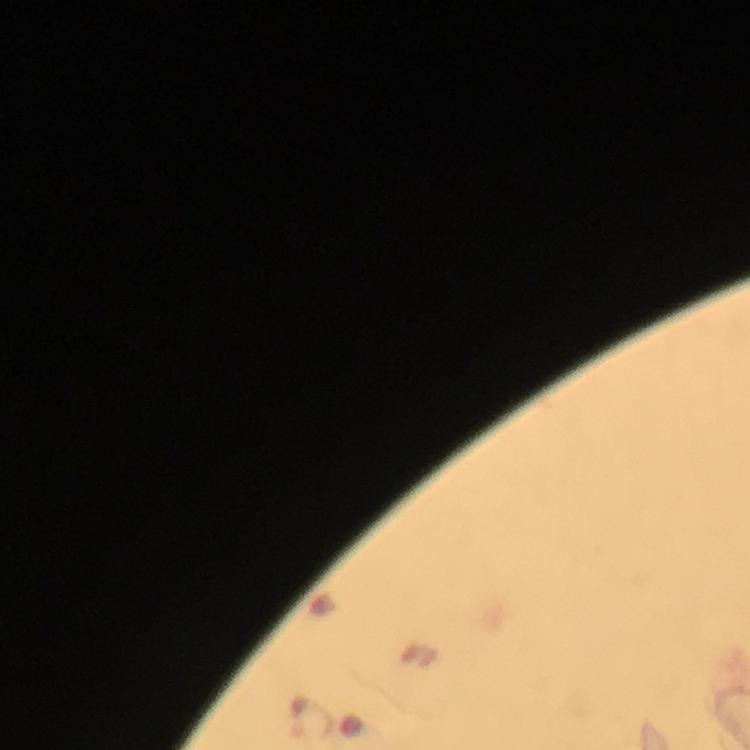
Approximate object centers, in pixels from the top-left corner.
Summary:
  - Malaria parasite locations: (x=310, y=718)
  - Preparation: thick smear
  - Stain: Giemsa
  - Immersion oil: applied
  - Cropped from: one field of view
  - Magnification: 100x
  - Image size: 750×750 pixels
  - Context: from a diagnostic examination for malaria
  - Capture: smartphone camera through the microscope